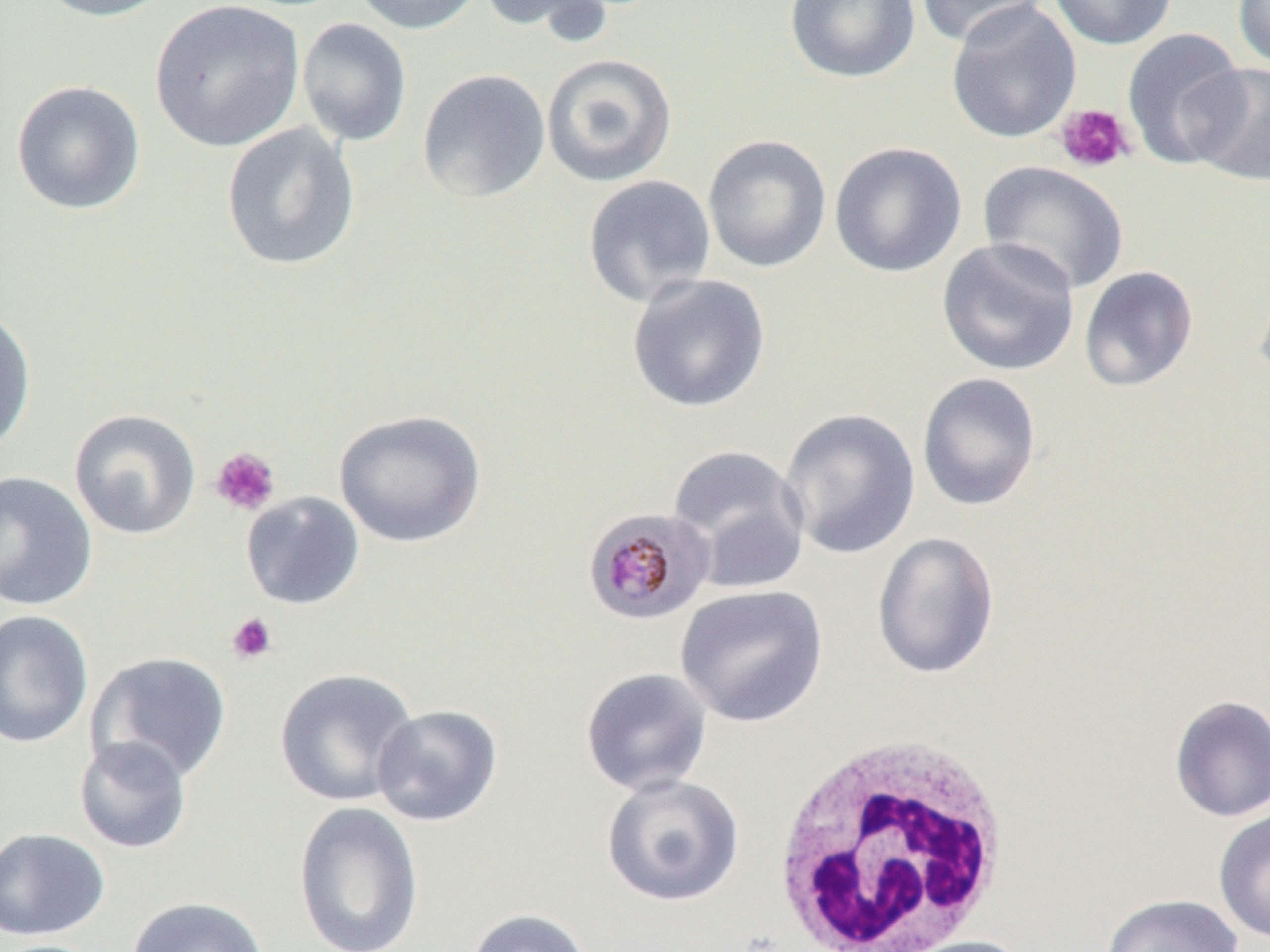

Approximate bounding boxes as (x1,y1)-(x2,y2) corner pairs in pixels. Uninfected red blood cell locations: (31,0)-(174,22), (349,0)-(485,35), (481,0)-(612,37), (784,0)-(921,83), (916,0)-(1052,47), (1048,0)-(1179,50), (1233,0)-(1270,71), (149,1)-(305,152), (945,1)-(1082,144), (296,17)-(413,146), (1122,28)-(1248,169), (541,52)-(677,187), (1186,62)-(1270,187), (416,69)-(551,204), (10,80)-(146,216), (221,122)-(361,271), (702,134)-(832,273), (829,141)-(967,278), (978,160)-(1129,295), (582,174)-(717,309), (936,237)-(1081,377), (1078,265)-(1199,393), (1253,268)-(1270,401), (627,274)-(770,414), (0,305)-(37,457), (917,372)-(1042,511), (69,408)-(202,540), (333,408)-(486,549), (779,408)-(921,559), (667,444)-(811,594), (0,470)-(98,611), (241,491)-(365,610), (872,532)-(1001,679), (675,584)-(828,727), (0,610)-(93,748), (86,652)-(232,785), (274,668)-(419,807), (580,668)-(712,796), (1168,694)-(1270,822), (372,704)-(503,827), (73,735)-(193,854), (601,773)-(744,907), (293,801)-(424,952), (1213,806)-(1270,944), (0,827)-(110,941), (1099,893)-(1244,952), (125,896)-(269,952), (463,908)-(594,952), (895,936)-(1033,952). Platelet locations: (1055,103)-(1135,173), (210,447)-(281,516), (226,612)-(278,665). Plasmodium malariae-infected red blood cell locations: (581,507)-(715,626). White blood cell locations: (766,733)-(1017,952). Slide-level diagnosis: Plasmodium malariae. Single field of view. Image is 1270×952 pixels. Captured at 1000x magnification. Optical microscopy. Thin blood smear.